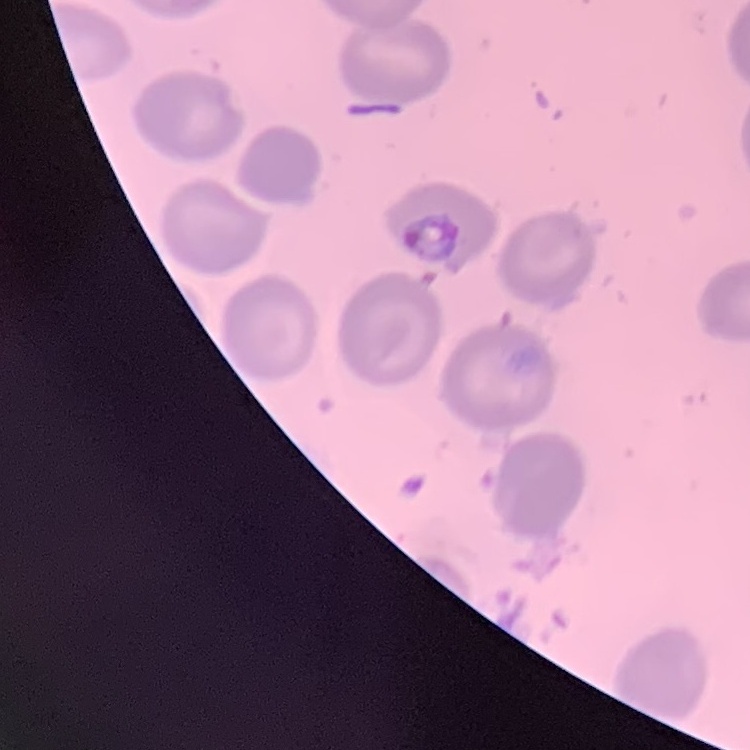 The red blood cells exhibit no rouleaux formation. One tile cut from a larger photomicrograph. Thin blood film. Stained with either Field's or Giemsa.